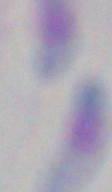
Summary:
  - Identification: Toxoplasma gondii
  - Modality: photomicrograph
  - Magnification: 1000x